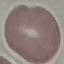

malaria status = uninfected
image type = cell patch, automatically extracted from a larger field of view and resized to 64 × 64 pixels
stain = Giemsa
capture = smartphone camera at the microscope eyepiece
preparation = thin blood film